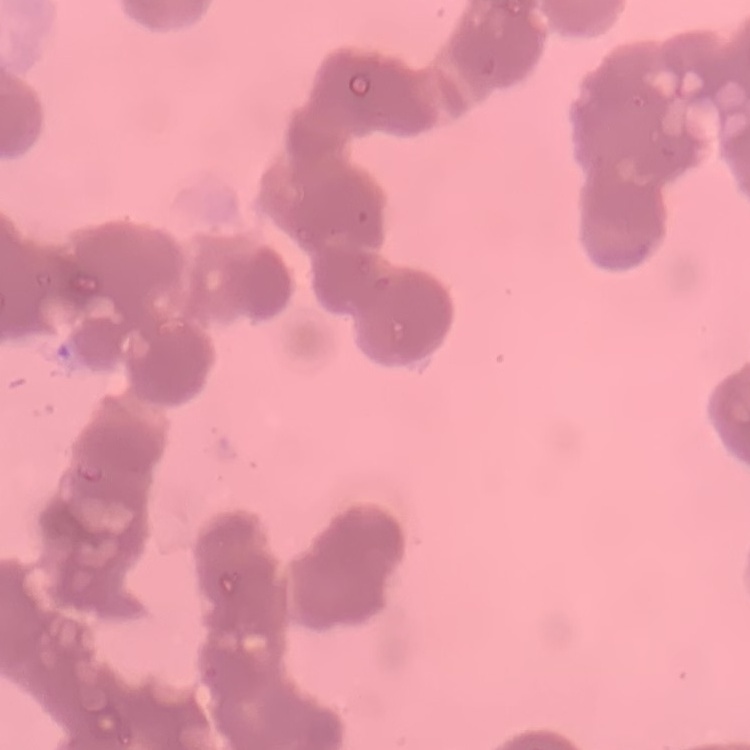 The red blood cells show rouleaux formation. One tile cut from a larger photomicrograph. Stained with either Field's or Giemsa. Thin peripheral smear.